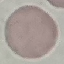
Summary:
  - Result: no malaria parasites detected
  - Capture: smartphone through the microscope eyepiece
  - Preparation: thin blood smear
  - Stain: Giemsa
  - Image type: automatically extracted cell patch, resized to 64 × 64 pixels